Locate every blood parasite and identify its species.
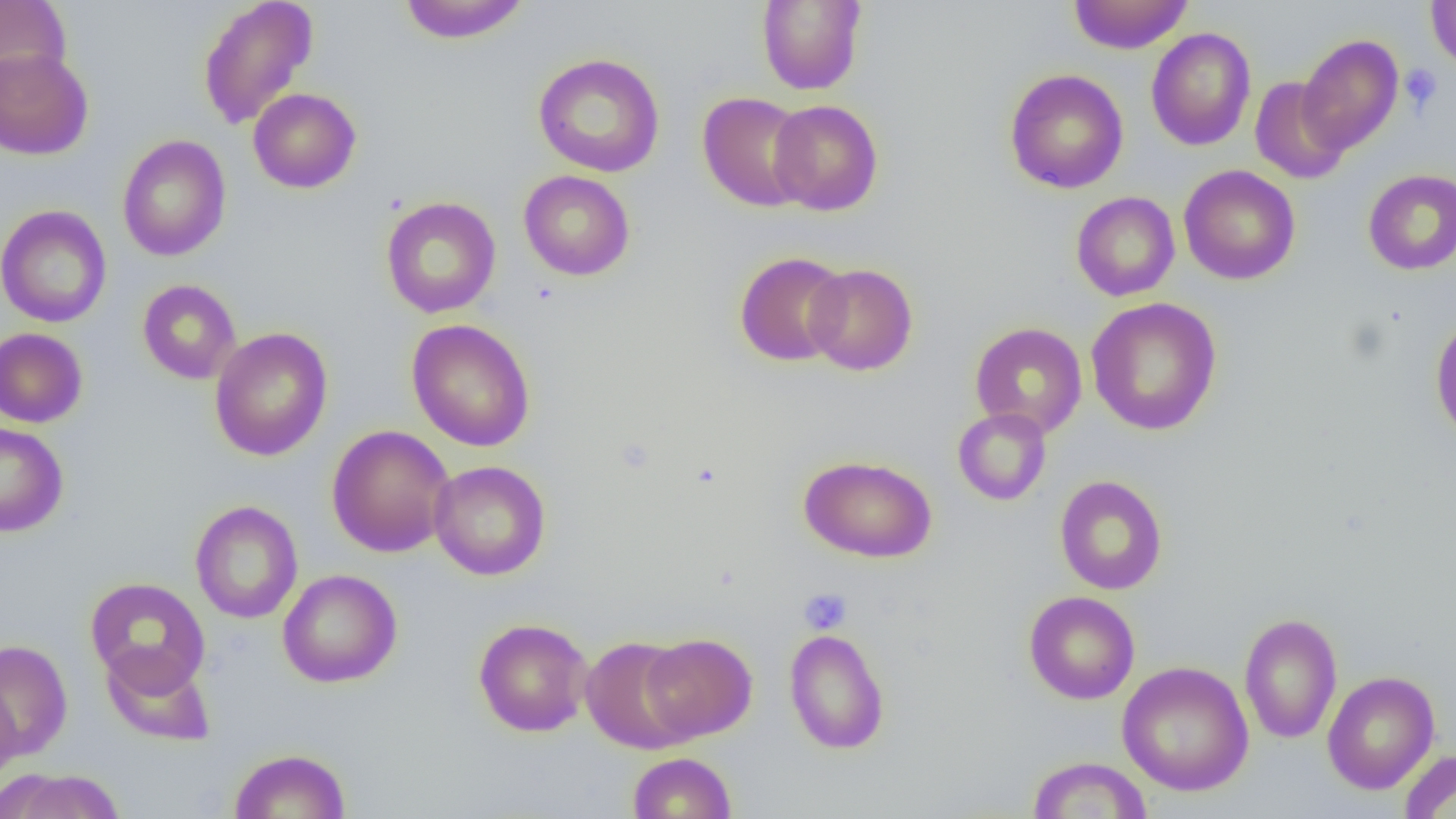

No blood parasites observed.

slide-level diagnosis = no evidence of blood parasites
preparation = thin blood smear
field of view = single
modality = light microscopy
magnification = 1000x
uninfected red blood cell locations = approximate bounding boxes as (x1, y1, x2, y2) in pixels: (0, 0, 71, 91), (197, 0, 318, 130), (397, 0, 530, 44), (1068, 0, 1192, 54), (756, 1, 866, 95), (1426, 1, 1456, 72), (1145, 27, 1256, 151), (1297, 34, 1404, 155), (0, 48, 94, 160), (533, 53, 665, 177), (1004, 68, 1129, 194), (1250, 76, 1350, 184), (248, 88, 361, 193), (698, 91, 813, 212), (769, 99, 883, 216), (117, 134, 231, 262), (1178, 165, 1301, 285), (1363, 169, 1456, 275), (519, 170, 635, 281), (1071, 191, 1180, 301), (381, 196, 501, 318), (0, 204, 112, 328), (733, 251, 850, 367), (804, 263, 918, 376), (137, 279, 241, 384), (1085, 297, 1223, 436), (1430, 313, 1456, 443), (406, 318, 536, 452), (969, 322, 1088, 438), (210, 327, 333, 461), (0, 328, 88, 428), (952, 407, 1052, 506), (0, 422, 69, 537), (326, 425, 455, 557), (799, 455, 937, 563), (429, 460, 551, 580), (1055, 475, 1168, 595), (190, 500, 303, 624), (277, 569, 402, 688), (85, 577, 211, 695), (1024, 591, 1140, 704), (1239, 611, 1342, 744), (473, 618, 593, 737), (784, 628, 890, 754), (640, 633, 757, 742), (581, 636, 697, 754), (0, 639, 73, 762), (100, 646, 216, 747), (1117, 661, 1254, 796), (1322, 670, 1440, 794), (0, 679, 21, 789), (229, 748, 351, 818), (1399, 749, 1456, 818), (628, 752, 737, 818), (1028, 756, 1152, 818), (3, 768, 127, 819)
platelet locations = approximate bounding boxes as (x1, y1, x2, y2) in pixels: (1399, 64, 1443, 114), (799, 587, 852, 633)
image size = 1456×819 pixels